Give the extent of all Plasmodium ovale-infected red blood cells.
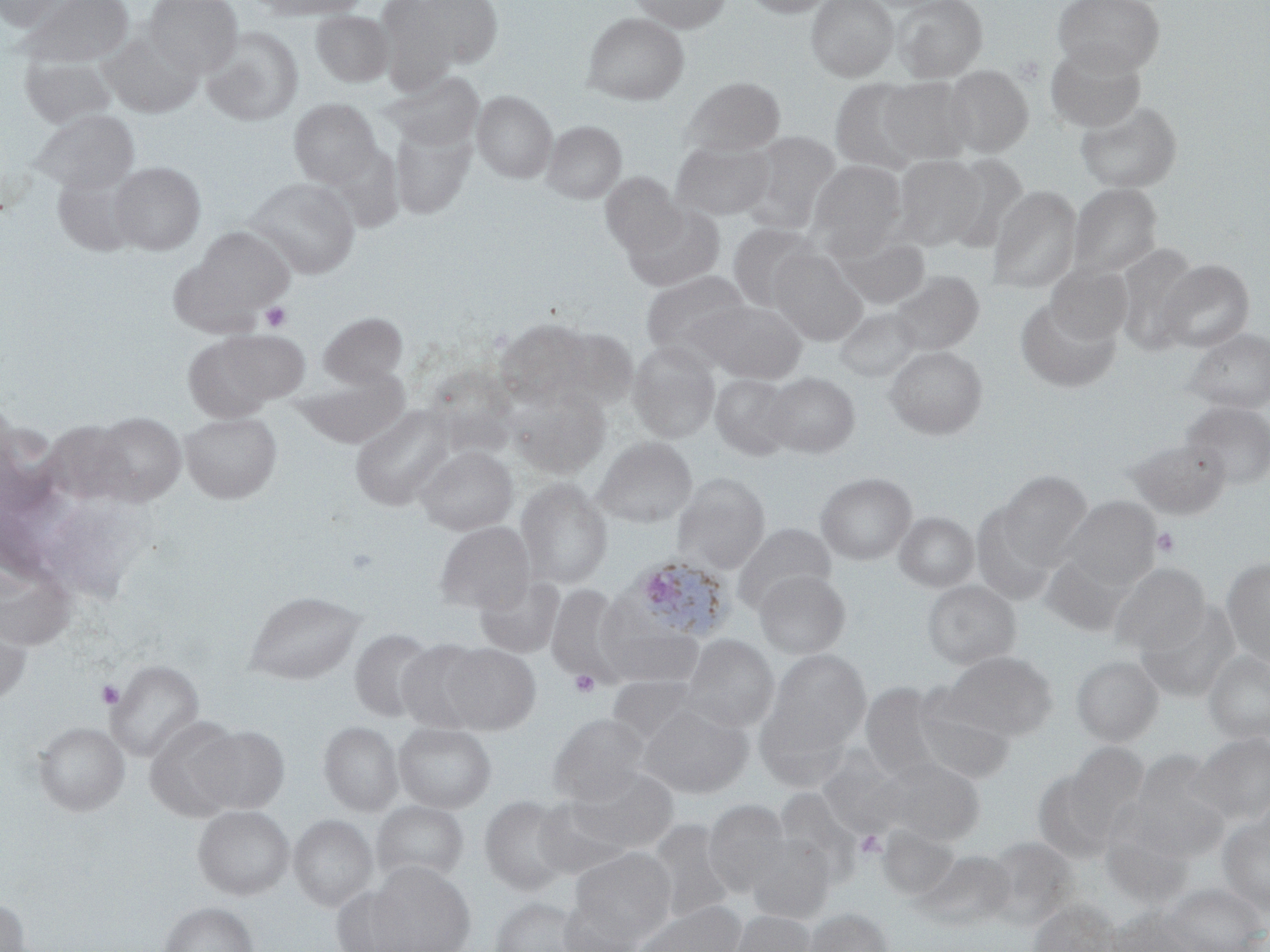
Approximate bounding boxes as (x1, y1, x2, y2) in pixels.
Plasmodium ovale-infected red blood cells: (626, 555, 736, 643).

{
  "slide_level_diagnosis": "Plasmodium ovale",
  "stain": "May-Grünwald-Giemsa",
  "platelet_locations": "approximate bounding boxes as (x1, y1, x2, y2) in pixels: (261, 302, 291, 331), (1152, 527, 1180, 557), (570, 669, 600, 697), (96, 680, 125, 709), (856, 831, 885, 859)",
  "magnification": "1000x",
  "field_of_view": "one of a larger specimen",
  "uninfected_red_blood_cell_locations": "approximate bounding boxes as (x1, y1, x2, y2) in pixels: (0, 0, 71, 31), (21, 0, 133, 66), (145, 0, 242, 77), (250, 0, 371, 19), (398, 0, 505, 71), (629, 0, 732, 33), (744, 0, 836, 17), (806, 0, 898, 81), (892, 0, 987, 83), (1052, 0, 1165, 76), (311, 10, 393, 87), (581, 12, 689, 105), (202, 27, 304, 126), (101, 32, 202, 118), (1044, 41, 1146, 132), (20, 54, 118, 128), (943, 65, 1033, 157), (385, 72, 484, 151), (682, 77, 785, 155), (879, 78, 972, 164), (830, 79, 926, 173), (472, 90, 556, 182), (289, 98, 381, 187), (1075, 101, 1182, 193), (28, 109, 139, 193), (542, 120, 626, 203), (391, 125, 475, 220), (741, 131, 842, 233), (670, 139, 775, 219), (893, 154, 986, 249), (944, 154, 1029, 252), (808, 160, 907, 249), (109, 161, 206, 254), (53, 171, 140, 256), (601, 173, 684, 257), (245, 177, 361, 278), (1068, 183, 1162, 278), (987, 186, 1082, 293), (622, 203, 726, 292), (727, 222, 819, 310), (193, 227, 294, 312), (832, 232, 931, 309), (1114, 243, 1199, 352), (768, 248, 867, 344), (1157, 259, 1255, 352), (1045, 263, 1133, 345), (640, 271, 752, 359), (889, 271, 984, 355), (1015, 297, 1121, 392), (701, 300, 807, 384), (835, 307, 922, 382), (319, 312, 407, 386), (495, 318, 592, 405), (555, 327, 637, 408), (1184, 328, 1269, 412), (182, 333, 296, 421), (627, 344, 720, 442), (884, 345, 988, 438), (300, 367, 411, 448), (764, 372, 860, 457), (710, 373, 794, 459), (508, 387, 610, 477), (1180, 400, 1270, 489), (351, 404, 456, 510), (92, 411, 186, 504), (180, 411, 282, 503), (47, 420, 134, 503), (594, 436, 697, 528), (1130, 437, 1230, 519), (416, 445, 517, 535), (998, 470, 1093, 565), (815, 472, 917, 564), (673, 473, 770, 574), (515, 478, 612, 589), (1061, 496, 1161, 589), (971, 505, 1056, 606), (895, 511, 979, 592), (435, 521, 535, 613), (733, 523, 836, 612), (1040, 552, 1134, 636), (1221, 557, 1270, 668), (0, 563, 76, 650), (1109, 563, 1210, 656), (753, 569, 851, 659), (475, 574, 565, 658), (922, 580, 1021, 670), (546, 584, 629, 685), (244, 590, 365, 684), (1137, 601, 1241, 702), (0, 609, 32, 706), (597, 611, 704, 690), (349, 629, 437, 722), (680, 634, 779, 730), (396, 640, 486, 733), (442, 643, 541, 734), (765, 650, 871, 754), (945, 650, 1058, 740), (1203, 650, 1270, 744), (1071, 656, 1163, 746), (106, 660, 204, 761), (605, 675, 711, 750), (860, 682, 946, 777), (912, 689, 1014, 784), (637, 700, 753, 798), (549, 713, 650, 805), (144, 717, 243, 821), (320, 721, 403, 815), (34, 722, 129, 815), (393, 722, 496, 813), (193, 726, 290, 813), (1189, 733, 1270, 825), (1066, 743, 1149, 831), (1133, 753, 1227, 852), (875, 757, 985, 845), (565, 766, 679, 857), (1033, 769, 1118, 862), (774, 787, 864, 886), (480, 795, 572, 894), (530, 798, 638, 879), (703, 799, 792, 897), (372, 800, 469, 885), (192, 805, 293, 899), (1217, 814, 1270, 915), (289, 815, 377, 910), (647, 819, 738, 923), (878, 824, 961, 900), (745, 834, 836, 923), (982, 835, 1078, 929), (570, 847, 676, 938), (915, 848, 1015, 930), (371, 862, 476, 952), (1158, 882, 1268, 952), (331, 885, 412, 952), (0, 896, 31, 952), (490, 896, 590, 952), (557, 897, 645, 952), (1028, 899, 1119, 952), (633, 900, 746, 952), (159, 901, 258, 952), (1105, 906, 1201, 951), (802, 907, 894, 952), (729, 910, 816, 952)",
  "preparation": "thin blood smear",
  "modality": "optical microscopy",
  "image_size": "1270×952 pixels"
}